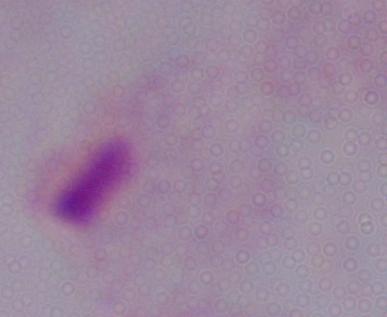

{
  "identification": "trichomonad",
  "modality": "photomicrograph",
  "magnification": "1000x"
}